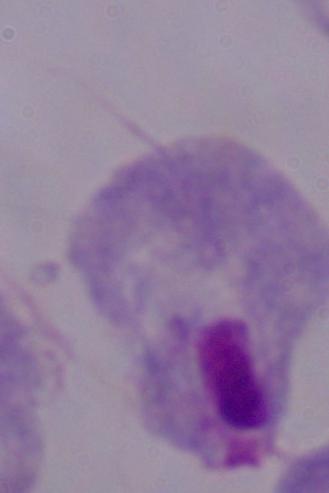 Captured at 1000x magnification. A trichomonad is shown. Photomicrograph.